Comment on the morphology of the red blood cells.
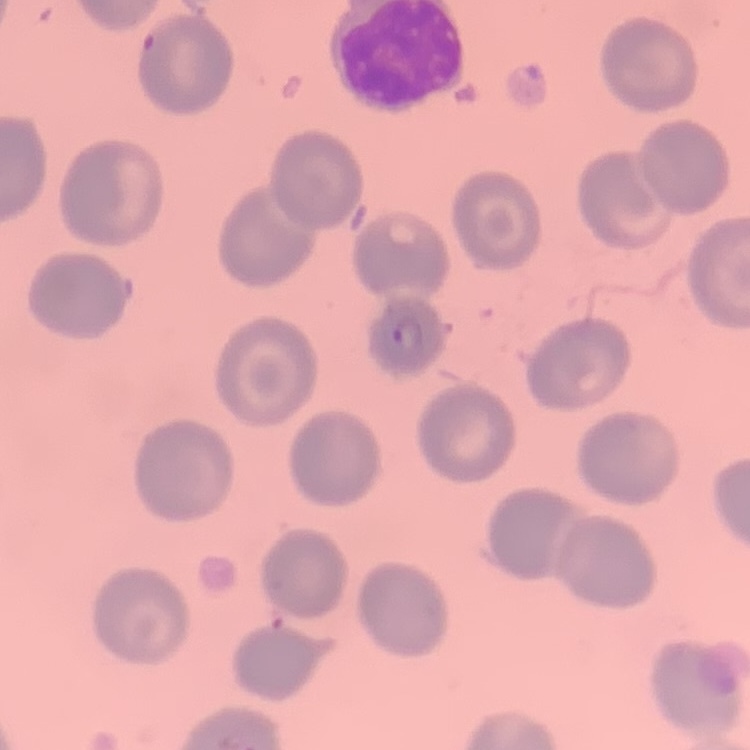

They show no rouleaux formation.

Square crop of a larger photomicrograph. Thin blood smear. Field's or Giemsa stain.